Describe the morphology of the red blood cells.
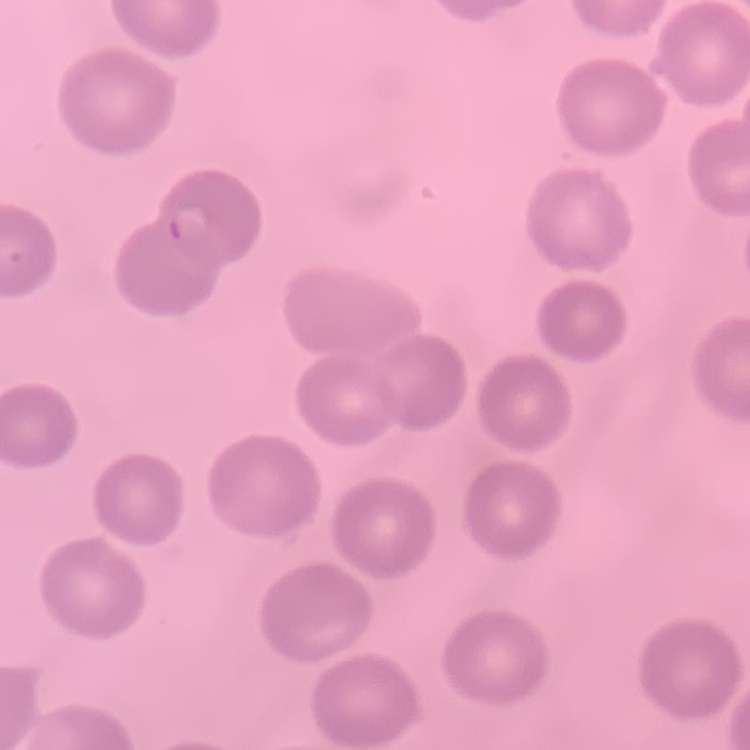

They show no rouleaux formation.

Summary:
  - Preparation: thin blood film
  - Image type: square crop of a larger photomicrograph
  - Stain: Field's or Giemsa